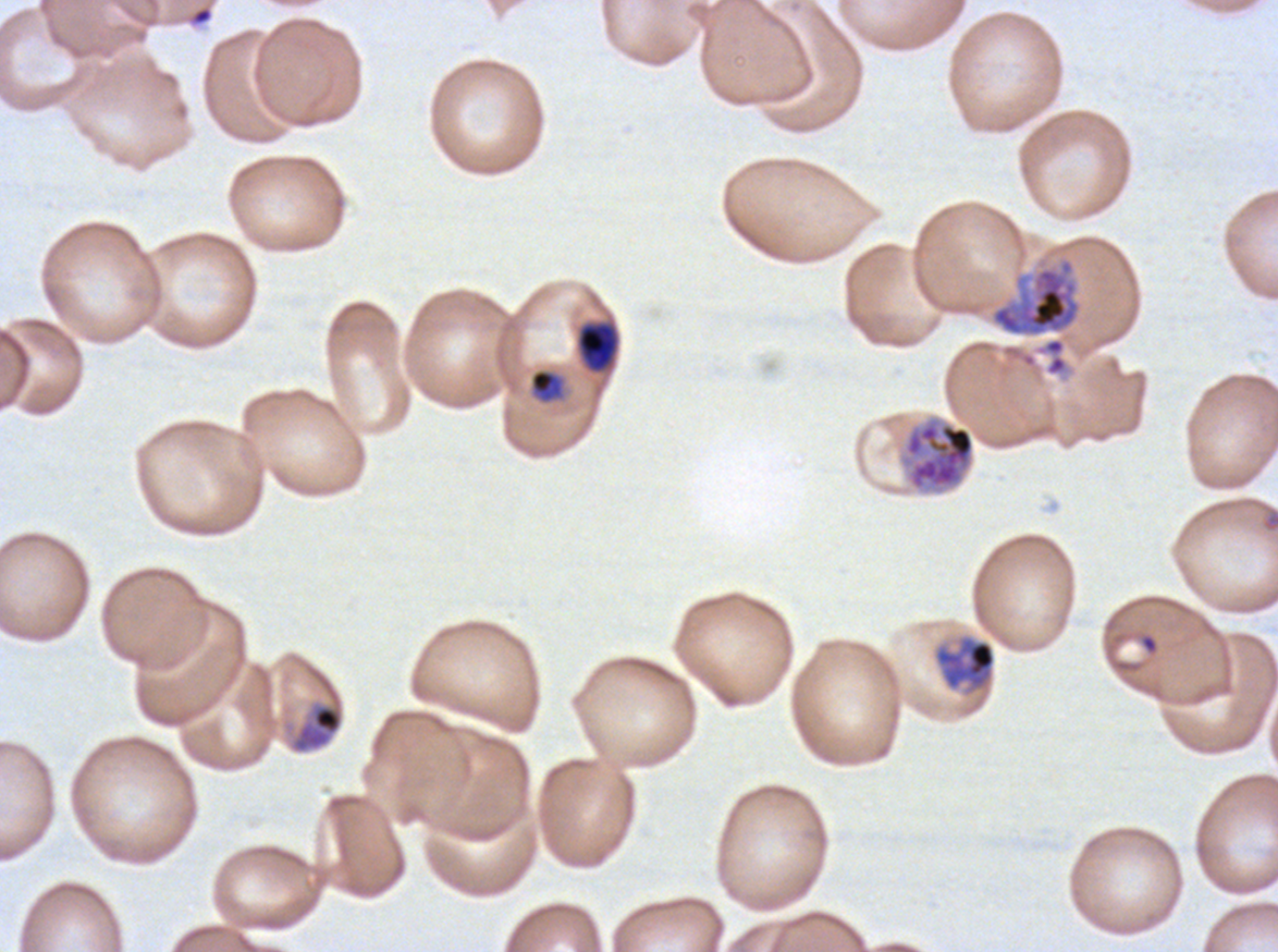
Approximate bounding boxes as {x1, y1, x2, y2} in pixels.
Summary:
  - Debris locations: {190, 6, 214, 26}
  - Object labeled both late-ring/early-trophozoite and mid trophozoite by the source: {575, 320, 621, 374}
  - Ring locations: {1139, 633, 1159, 654}
  - Late schizont locations: {900, 415, 976, 494}
  - Mid trophozoite locations: {934, 637, 996, 690}, {292, 703, 343, 752}
  - Late trophozoite locations: {989, 257, 1083, 337}
  - Preparation: thin blood film
  - Life-cycle stages observed: ring, mid trophozoite, late trophozoite, late schizont
  - Stain: Giemsa
  - Specimen: Plasmodium falciparum cultured ex vivo for 24 to 48 hours, from a patient in The Gambia
  - Field of view: sub-image separated from a larger composite
  - Image size: 1278×952 pixels